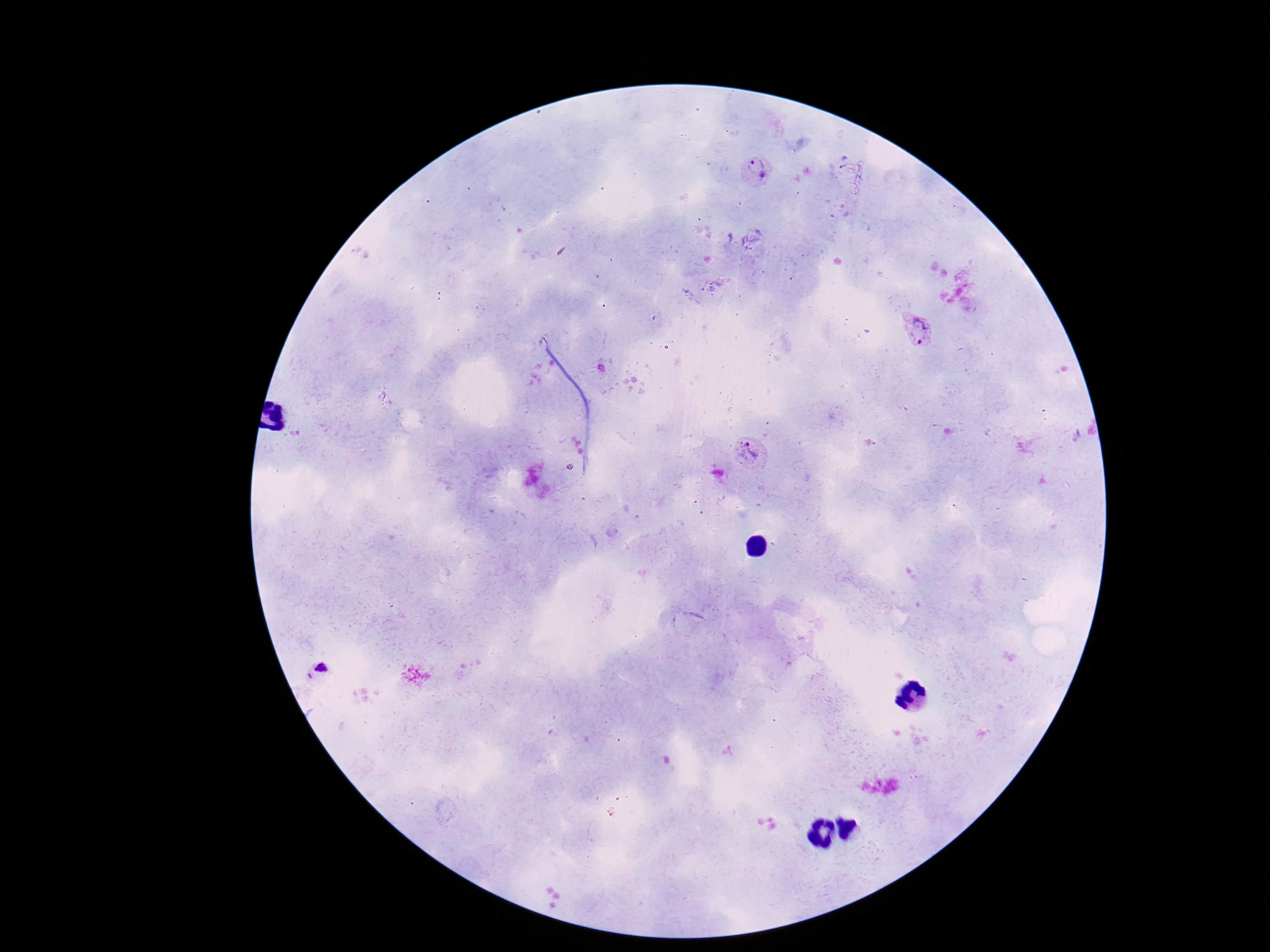
Approximate centers as (x, y) in pixels.
Summary:
  - Plasmodium parasite locations: (754, 171), (918, 330), (748, 453), (318, 674)
  - Patient malaria status: positive
  - Image size: 1270×952 pixels
  - Magnification: 100x
  - Capture: smartphone camera through the microscope eyepiece
  - Preparation: thick blood film
  - Field of view: single
  - Stain: Giemsa